Classify this cell by malaria status.
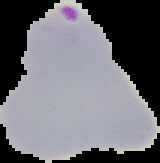

It is parasitized.

Summary:
  - Preparation: thin blood smear
  - Image size: 160×163 pixels
  - Image type: segmented cell region with the area outside set to black